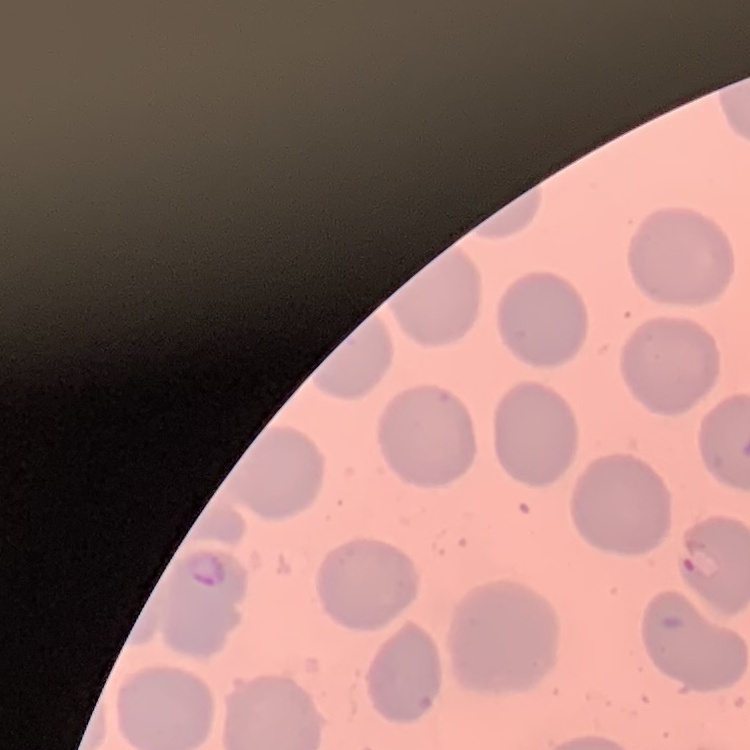
red blood cell morphology = no rouleaux formation
stain = Field's or Giemsa
image type = square crop of a larger photomicrograph
preparation = thin blood smear